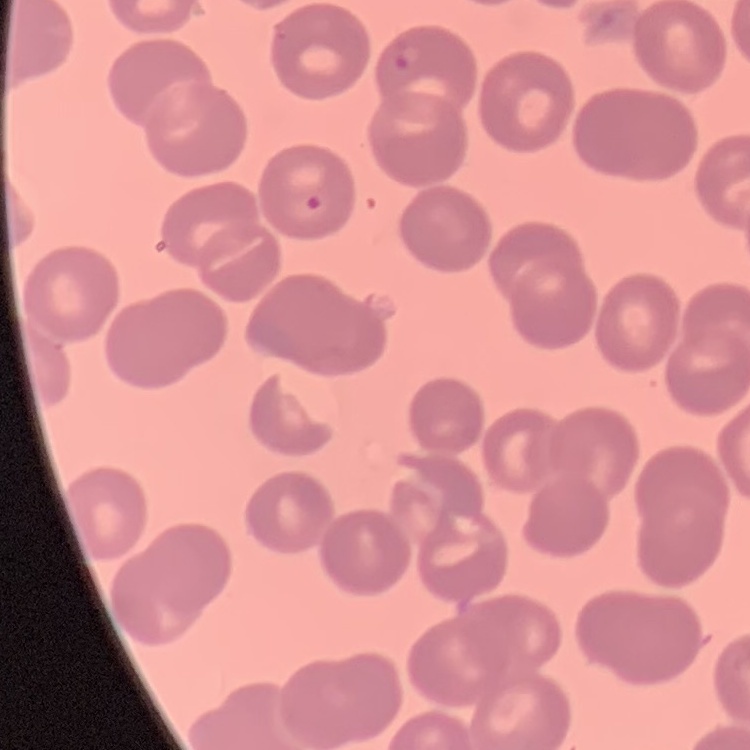
The red blood cells show no rouleaux formation. One tile cut from a larger photomicrograph. Field's or Giemsa stain. Thin peripheral smear.